Outline each blood parasite and name the species.
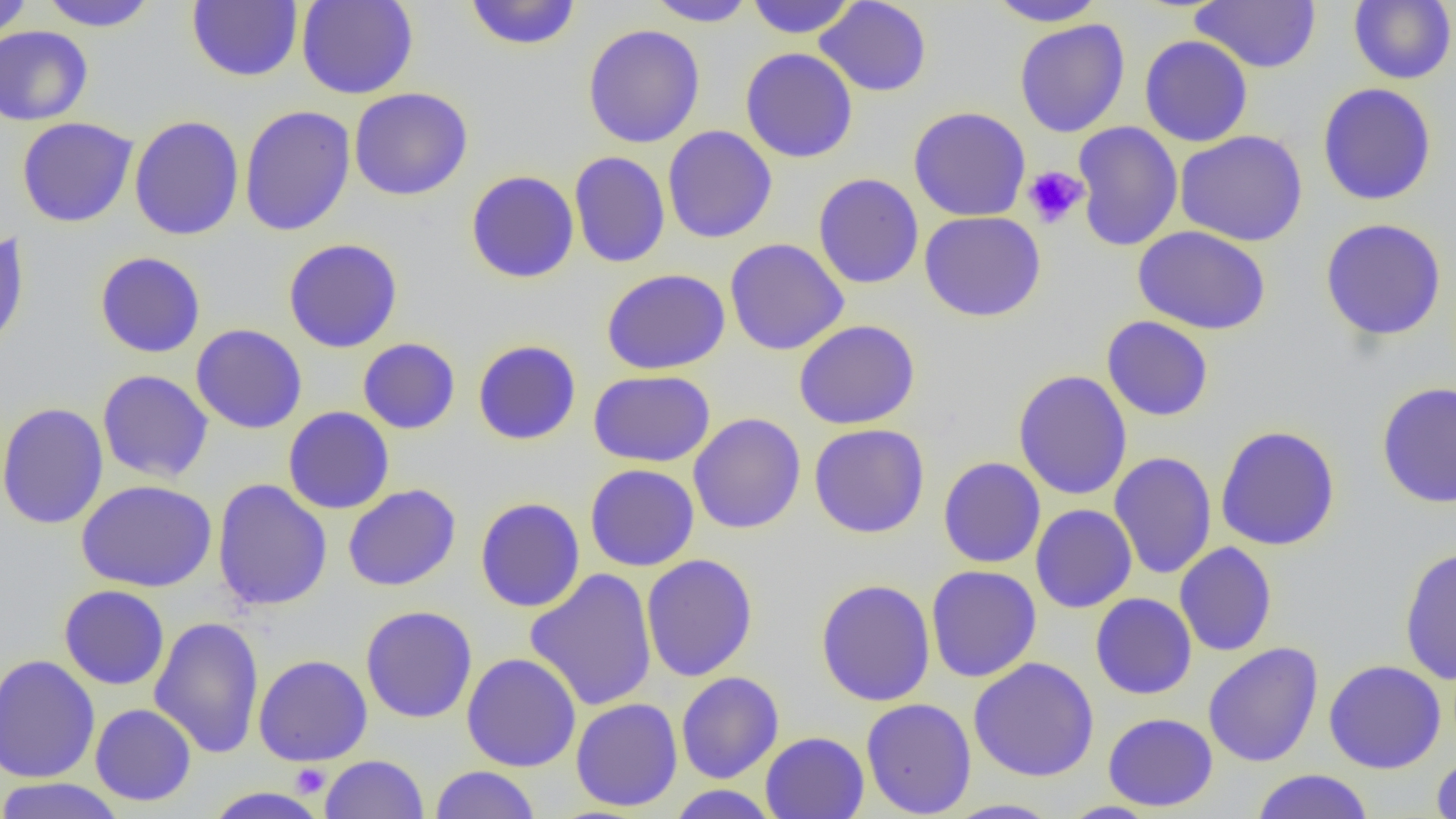

No blood parasites observed.

Approximate bounding boxes as [x1, y1, x2, y2] in pixels. Uninfected red blood cell locations: [0, 0, 34, 40], [38, 0, 159, 31], [296, 0, 419, 99], [464, 0, 581, 51], [645, 0, 758, 27], [746, 0, 857, 38], [985, 0, 1107, 27], [1348, 0, 1456, 85], [187, 1, 303, 82], [815, 1, 932, 97], [1191, 1, 1321, 73], [1014, 19, 1130, 137], [583, 23, 706, 148], [0, 26, 93, 126], [1139, 35, 1253, 147], [740, 47, 859, 163], [1317, 83, 1437, 206], [348, 87, 474, 201], [239, 105, 356, 236], [908, 106, 1031, 222], [129, 115, 245, 241], [15, 117, 139, 228], [1072, 121, 1183, 252], [662, 125, 777, 243], [1175, 129, 1308, 246], [569, 151, 670, 268], [466, 170, 579, 284], [813, 173, 924, 289], [919, 210, 1046, 322], [1320, 218, 1447, 341], [1133, 226, 1271, 335], [0, 228, 30, 355], [283, 238, 403, 353], [724, 238, 849, 355], [94, 251, 206, 358], [601, 268, 731, 374], [1101, 315, 1214, 421], [793, 319, 920, 429], [191, 323, 308, 434], [358, 337, 460, 434], [472, 339, 581, 445], [1013, 369, 1133, 501], [97, 370, 213, 483], [588, 370, 716, 467], [1375, 382, 1456, 508], [0, 401, 109, 530], [283, 406, 395, 514], [688, 412, 806, 534], [809, 423, 930, 538], [1215, 425, 1341, 551], [1109, 452, 1217, 579], [938, 456, 1046, 569], [585, 464, 699, 572], [212, 479, 333, 611], [77, 480, 217, 592], [342, 484, 461, 592], [474, 497, 585, 612], [1031, 504, 1137, 613], [1174, 541, 1278, 657], [1398, 544, 1456, 685], [641, 554, 758, 682], [926, 565, 1042, 682], [525, 568, 658, 711], [815, 578, 936, 706], [58, 584, 170, 690], [1090, 593, 1197, 700], [360, 605, 478, 723], [149, 616, 265, 759], [1203, 642, 1324, 767], [461, 652, 581, 772], [0, 654, 100, 784], [253, 654, 373, 766], [969, 657, 1099, 782], [1324, 659, 1446, 774], [676, 671, 784, 783], [861, 697, 976, 817], [570, 698, 683, 812], [90, 703, 196, 806], [1103, 712, 1218, 811], [760, 731, 869, 819], [1431, 753, 1456, 817], [320, 754, 429, 818], [429, 765, 541, 819], [1251, 769, 1374, 819], [0, 777, 126, 819], [667, 785, 779, 818], [202, 786, 329, 819], [942, 798, 1065, 818], [1056, 801, 1162, 818]. Platelet locations: [1022, 166, 1089, 229], [290, 763, 330, 797]. Slide-level diagnosis: no evidence of blood parasites. Thin blood film. Image is 1456×819 pixels. 1000x magnification. One field of a larger specimen. Optical microscopy.